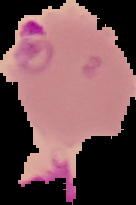

The area outside the segmented cell region is set to black. Image is 136×205 pixels. From a thin blood smear. Malaria status: parasitized.